Identify the preparation type.
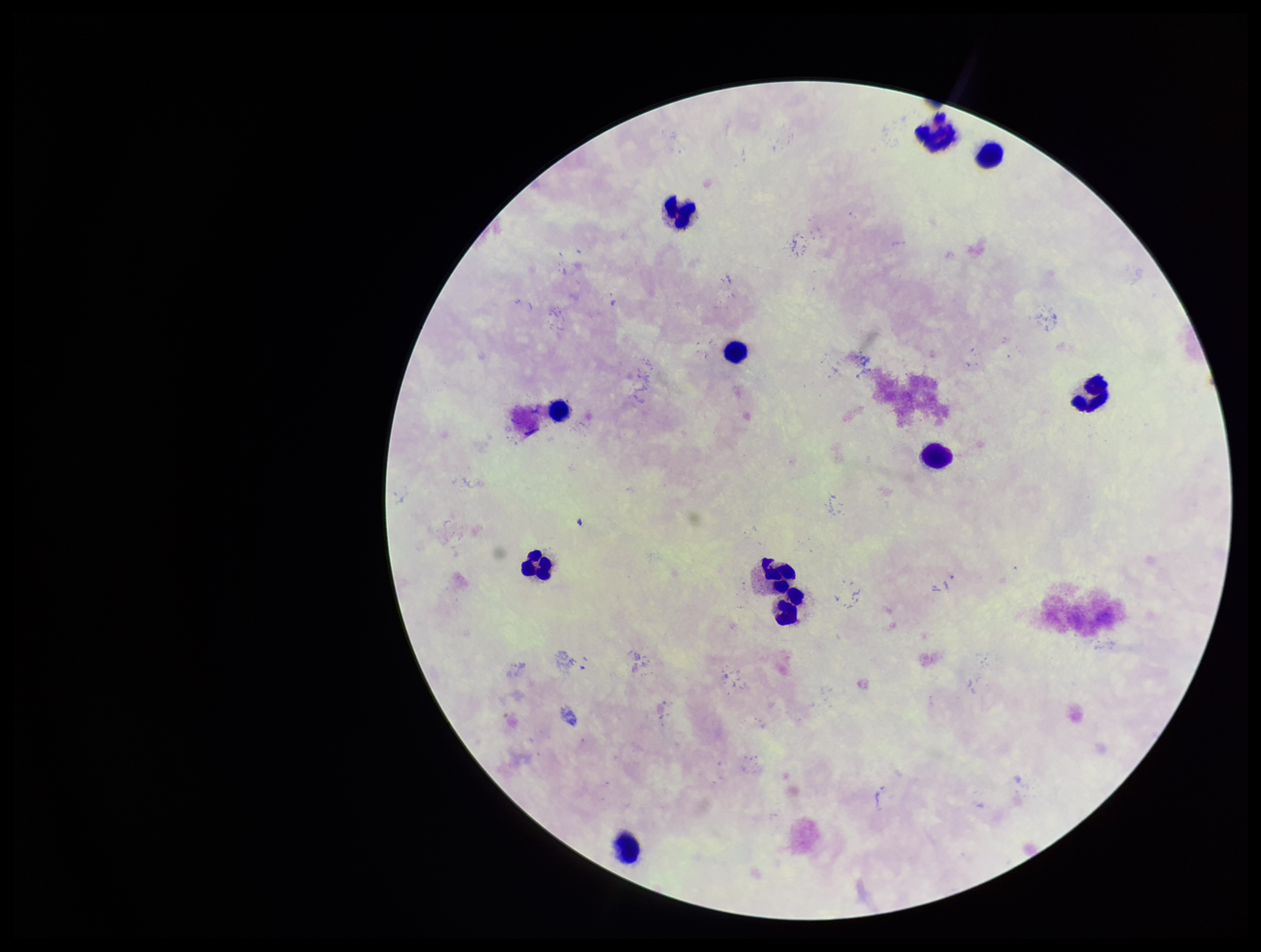

It is a thick blood smear.

Patient malaria status: negative. Parasite count: 0. One field from this slide. Image is 1261×952 pixels. Leukocyte count: 11. Photographed through the microscope eyepiece with a smartphone camera. Plasmodium parasites: none identified. Giemsa stain.